Assess the morphology of the erythrocytes.
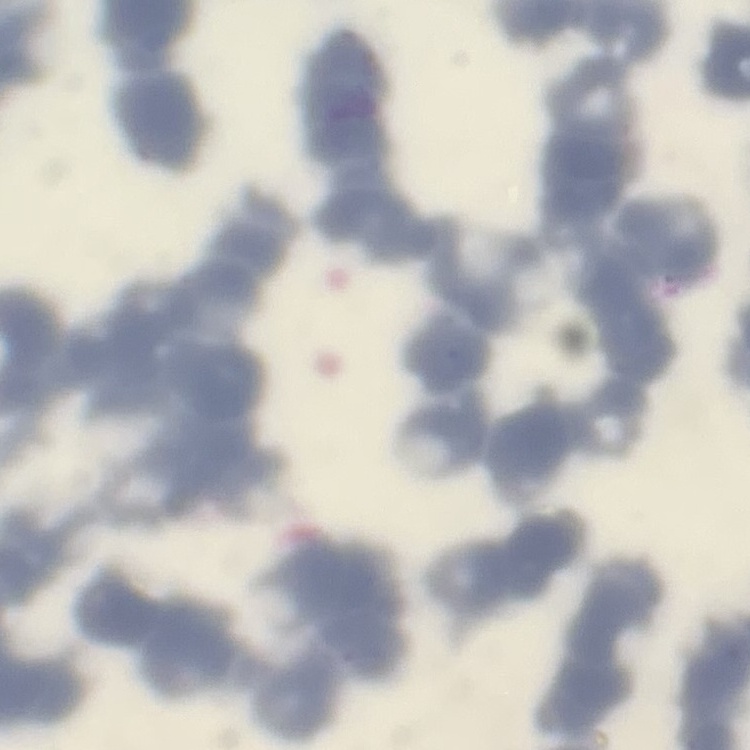
Rouleaux formation.

Thin peripheral smear. One tile cut from a larger photomicrograph. Stained with either Field's or Giemsa.